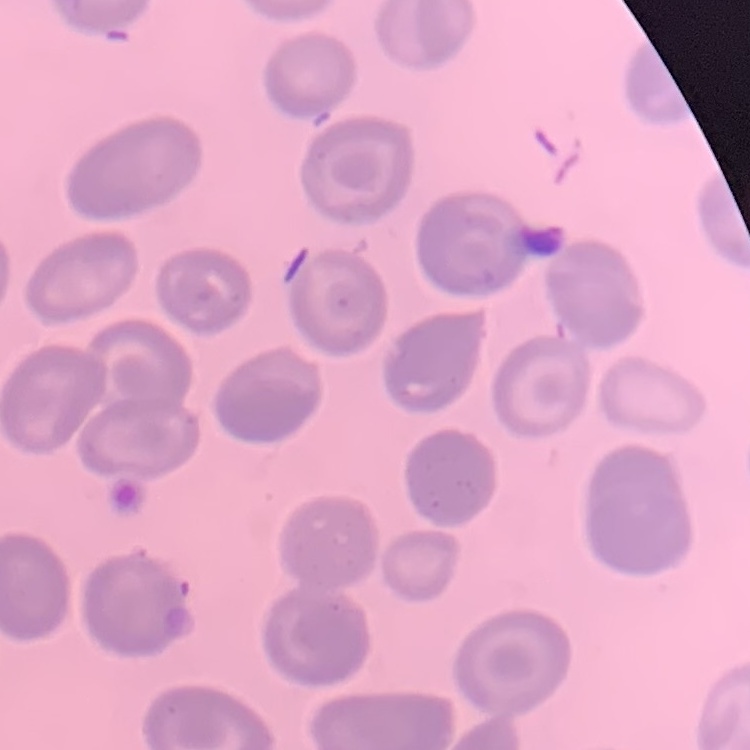

Summary:
  - Erythrocyte morphology: no rouleaux formation
  - Image type: one tile cut from a larger photomicrograph
  - Preparation: thin blood film
  - Stain: Field's or Giemsa